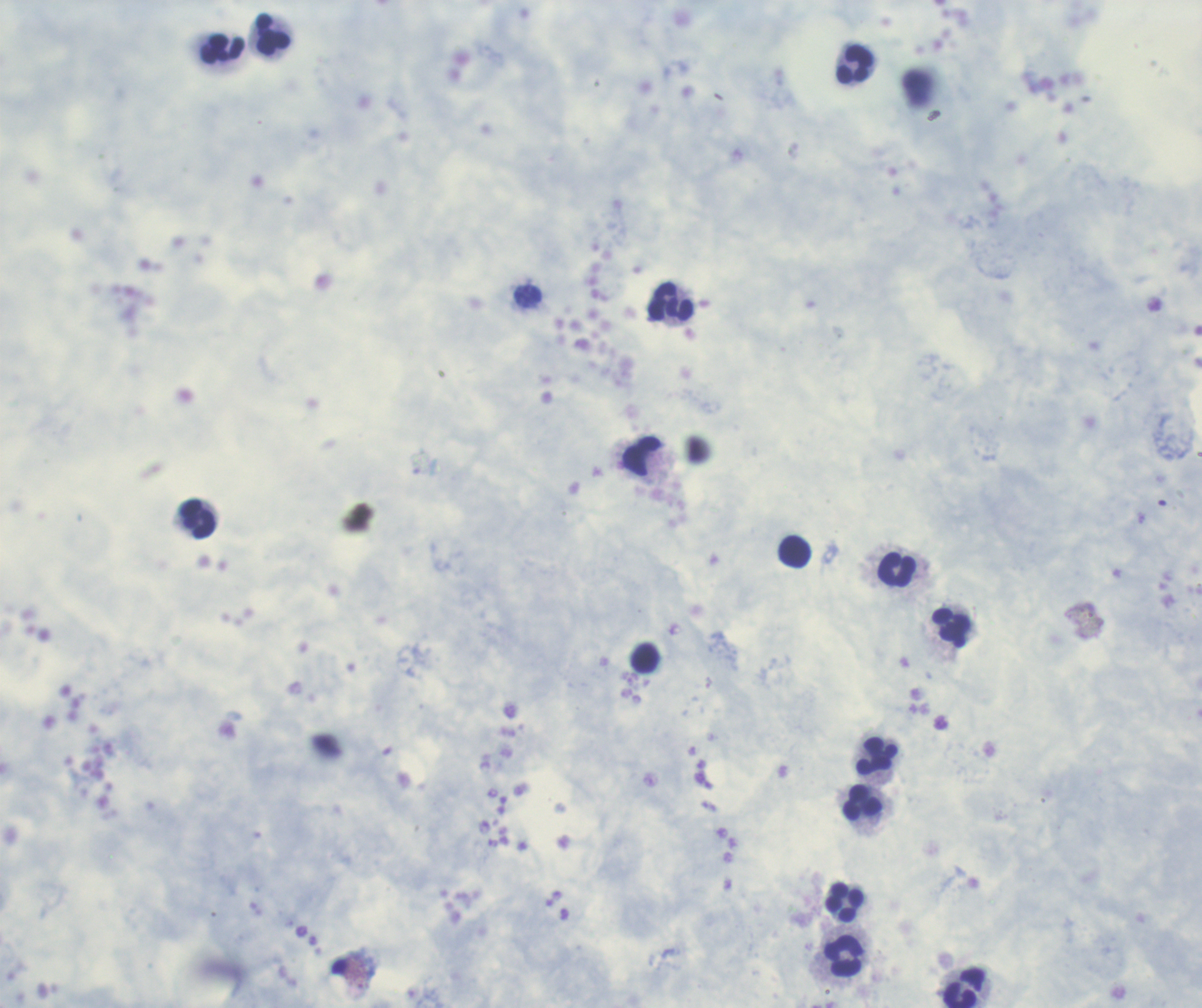

coordinate format = approximate centers as (x, y) in pixels
leukocyte locations = (272, 35), (223, 49), (854, 66), (672, 303), (642, 458), (198, 520), (795, 552), (897, 570), (950, 628), (645, 659), (878, 757), (863, 803), (844, 902), (845, 957), (964, 988)
coloration quality = good
result = no Plasmodium parasites detected
field of view = one from this slide
image size = 1202×1008 pixels
magnification = 100x
stain = Romanowsky
background quality = satisfactory
context = previously used in a real diagnosis
preparation = thick smear of blood